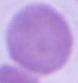

Summary:
  - Identification: red blood cell
  - Modality: micrograph
  - Magnification: 1000x